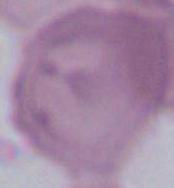 1000x magnification. An erythrocyte is shown. Photomicrograph.